Name the parasite shown.
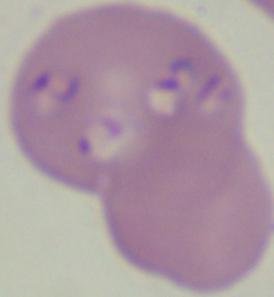

Babesia.

modality = photomicrograph
magnification = 1000x